Give the preparation type.
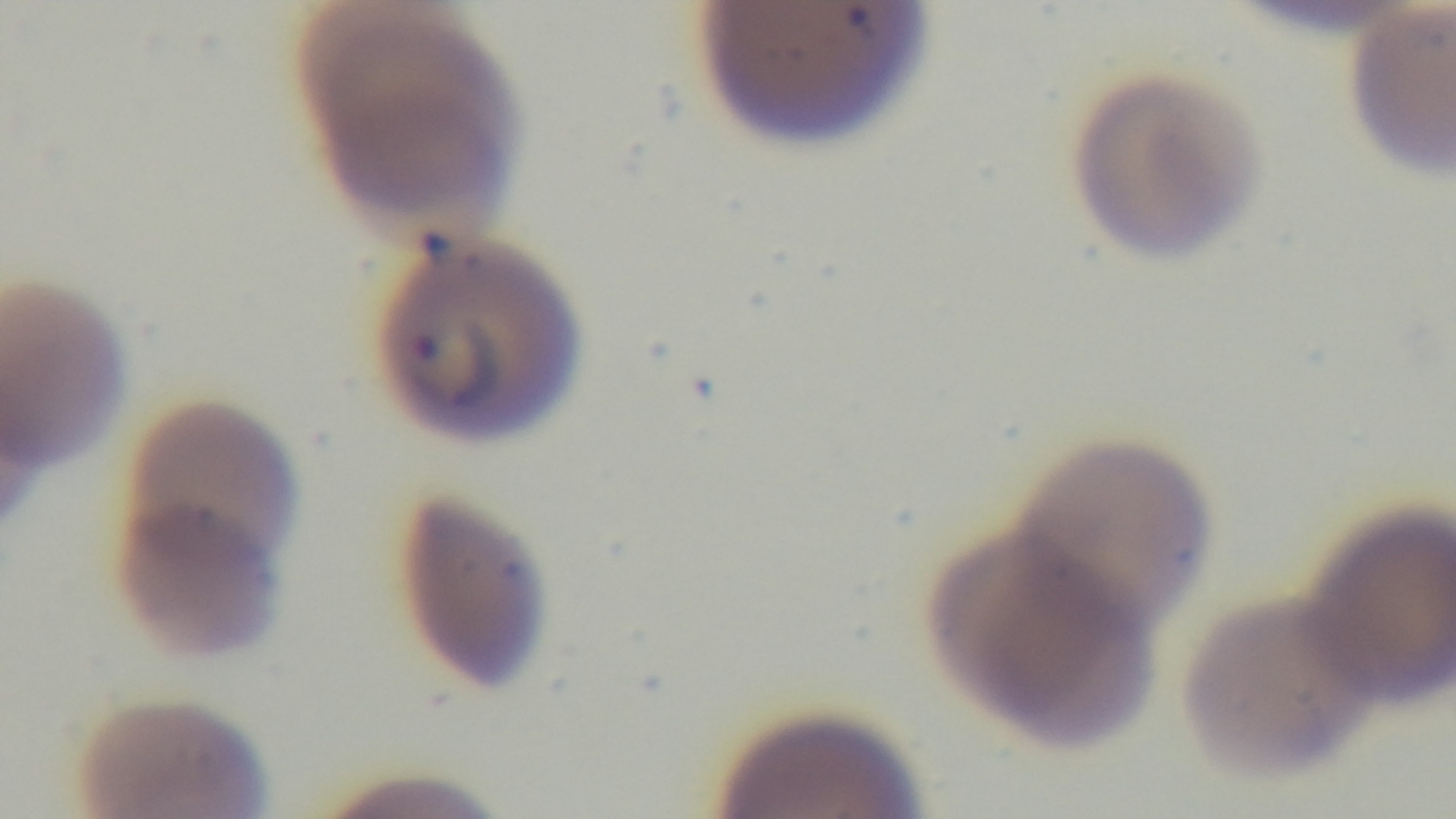

It is a thin blood film.

Summary:
  - Malaria status: positive
  - Objective: 100x oil immersion
  - Capture: mounted 4K digital camera
  - Field of view: single
  - Modality: light microscopy
  - Stain: Giemsa